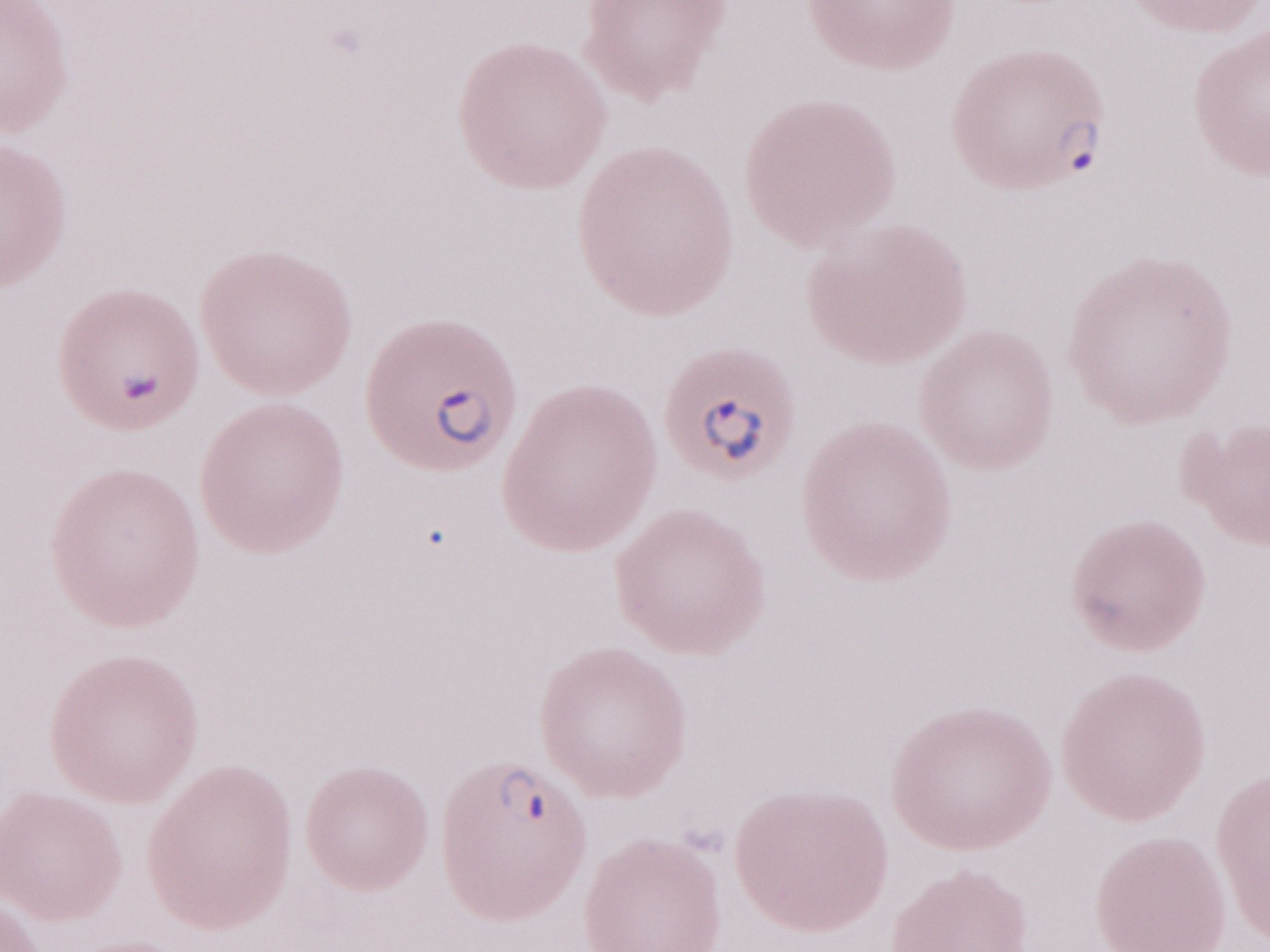 Malaria diagnosis (patient-level): positive. One field of this slide. Image is 1270×952 pixels. Thin peripheral-blood smear. Olympus BX43 microscope, Olympus DP73 camera. May-Grünwald-Giemsa-stained preparation. Magnification: 1,000x.